Assess this cell for malaria.
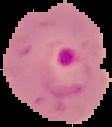

Parasitized.

Summary:
  - Image size: 112×127 pixels
  - Preparation: thin blood film
  - Image type: segmented cell region on a black background